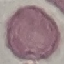

Result: no malaria parasites detected. Giemsa-stained preparation. Thin blood smear. Automatically extracted cell patch, resized to 64 × 64 pixels. Photographed with a smartphone camera at the microscope eyepiece.